Point out every Plasmodium parasite and every leukocyte.
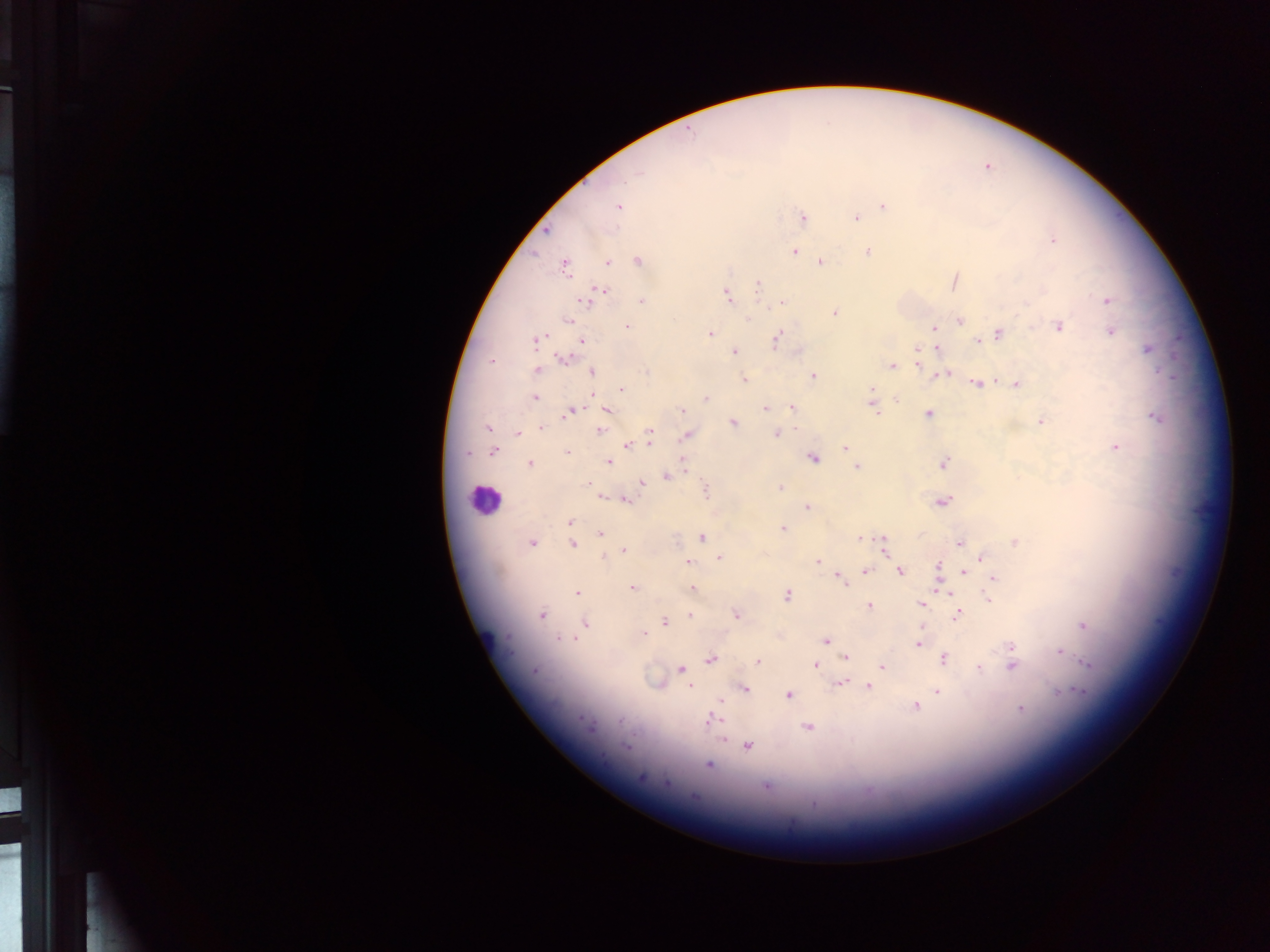

Approximate centers as {x, y} in pixels.
Plasmodium parasites: {689, 133}, {636, 174}, {883, 205}, {619, 206}, {801, 217}, {854, 217}, {1054, 241}, {795, 250}, {866, 250}, {638, 260}, {821, 261}, {608, 262}, {564, 266}, {758, 285}, {596, 293}, {725, 295}, {641, 300}, {1107, 300}, {776, 305}, {833, 311}, {749, 319}, {572, 320}, {960, 321}, {1058, 326}, {628, 327}, {933, 328}, {1111, 329}, {778, 333}, {998, 333}, {709, 334}, {536, 340}, {580, 340}, {976, 341}, {776, 343}, {916, 349}, {937, 349}, {1149, 349}, {733, 351}, {565, 359}, {919, 364}, {892, 366}, {536, 371}, {592, 372}, {814, 376}, {743, 378}, {976, 384}, {1016, 384}, {871, 388}, {622, 389}, {590, 392}, {897, 398}, {535, 399}, {705, 399}, {765, 408}, {790, 408}, {573, 409}, {681, 410}, {607, 411}, {875, 412}, {928, 413}, {1041, 420}, {733, 424}, {542, 427}, {486, 429}, {599, 430}, {775, 433}, {517, 434}, {649, 435}, {685, 435}, {626, 446}, {1116, 448}, {846, 449}, {494, 451}, {466, 453}, {567, 453}, {680, 457}, {814, 459}, {530, 463}, {606, 463}, {943, 463}, {858, 465}, {684, 467}, {665, 477}, {586, 483}, {641, 483}, {780, 488}, {705, 489}, {600, 497}, {625, 500}, {943, 502}, {807, 506}, {569, 521}, {783, 529}, {600, 535}, {702, 537}, {860, 537}, {883, 539}, {959, 542}, {1016, 542}, {534, 544}, {574, 544}, {883, 548}, {624, 550}, {980, 556}, {719, 557}, {818, 561}, {688, 562}, {939, 567}, {866, 570}, {901, 572}, {964, 574}, {840, 578}, {993, 578}, {845, 583}, {938, 583}, {631, 588}, {693, 588}, {577, 593}, {787, 595}, {949, 596}, {989, 599}, {922, 604}, {868, 605}, {542, 614}, {689, 614}, {957, 614}, {736, 615}, {584, 623}, {664, 623}, {1085, 626}, {643, 632}, {574, 638}, {826, 640}, {916, 645}, {1012, 646}, {1058, 651}, {844, 657}, {943, 657}, {712, 660}, {757, 661}, {1086, 662}, {814, 664}, {1011, 666}, {881, 668}, {977, 669}, {534, 670}, {679, 670}, {843, 682}, {838, 684}, {868, 687}, {690, 688}, {746, 689}, {1081, 691}, {938, 692}, {1060, 693}, {788, 694}, {721, 701}, {914, 706}, {1020, 708}, {712, 718}, {589, 726}, {805, 726}, {721, 741}, {626, 748}, {748, 748}, {709, 766}, {640, 776}, {667, 783}, {766, 788}, {868, 793}.
Leukocytes: {483, 500}.

field_of_view: single
image_size: 1270×952 pixels
capture: mobile-phone photograph through a microscope
country: Ghana
preparation: thick blood film